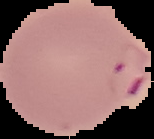

Summary:
  - Malaria status: parasitized
  - Image size: 154×139 pixels
  - Preparation: thin blood film
  - Image type: cell region segmented out of the field of view; surrounding area masked to black